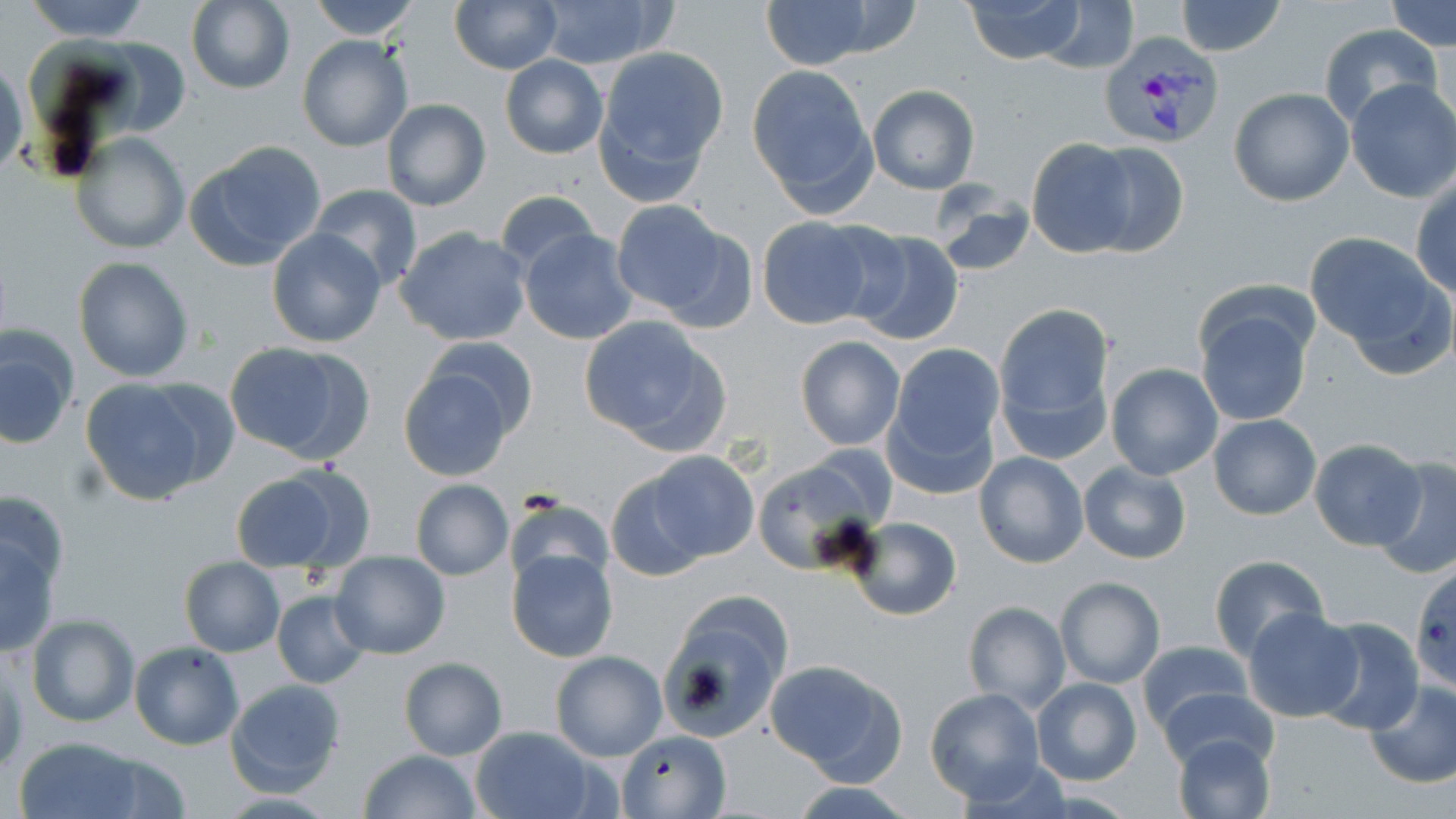

Approximate bounding boxes as named x1/y1/x2/y2 corners in pixels. Uninfected red blood cell locations: (x1=22, y1=0, x2=155, y2=41), (x1=308, y1=0, x2=422, y2=40), (x1=531, y1=0, x2=675, y2=70), (x1=964, y1=0, x2=1088, y2=64), (x1=1173, y1=0, x2=1288, y2=56), (x1=186, y1=1, x2=294, y2=93), (x1=449, y1=1, x2=560, y2=73), (x1=757, y1=1, x2=882, y2=70), (x1=1034, y1=1, x2=1141, y2=74), (x1=1386, y1=1, x2=1455, y2=50), (x1=1317, y1=23, x2=1442, y2=129), (x1=297, y1=35, x2=415, y2=153), (x1=593, y1=45, x2=729, y2=190), (x1=500, y1=55, x2=608, y2=158), (x1=1, y1=56, x2=26, y2=184), (x1=746, y1=64, x2=878, y2=213), (x1=1344, y1=80, x2=1456, y2=203), (x1=866, y1=85, x2=980, y2=194), (x1=1228, y1=89, x2=1353, y2=207), (x1=381, y1=98, x2=492, y2=211), (x1=72, y1=133, x2=189, y2=254), (x1=1027, y1=138, x2=1133, y2=255), (x1=186, y1=141, x2=328, y2=269), (x1=1083, y1=141, x2=1189, y2=258), (x1=1411, y1=177, x2=1456, y2=301), (x1=930, y1=183, x2=1034, y2=278), (x1=308, y1=185, x2=423, y2=294), (x1=495, y1=190, x2=601, y2=276), (x1=610, y1=200, x2=742, y2=323), (x1=756, y1=217, x2=884, y2=329), (x1=266, y1=227, x2=388, y2=348), (x1=395, y1=227, x2=530, y2=346), (x1=520, y1=228, x2=638, y2=344), (x1=843, y1=229, x2=965, y2=347), (x1=1304, y1=232, x2=1450, y2=365), (x1=73, y1=256, x2=196, y2=383), (x1=991, y1=300, x2=1117, y2=463), (x1=1195, y1=306, x2=1313, y2=429), (x1=578, y1=314, x2=729, y2=452), (x1=1, y1=328, x2=77, y2=449), (x1=416, y1=334, x2=542, y2=445), (x1=794, y1=337, x2=906, y2=451), (x1=224, y1=340, x2=374, y2=465), (x1=889, y1=344, x2=1005, y2=463), (x1=397, y1=361, x2=520, y2=481), (x1=1106, y1=364, x2=1223, y2=481), (x1=80, y1=377, x2=231, y2=506), (x1=1209, y1=415, x2=1322, y2=520), (x1=1308, y1=439, x2=1427, y2=552), (x1=645, y1=451, x2=759, y2=564), (x1=975, y1=451, x2=1087, y2=568), (x1=752, y1=457, x2=882, y2=574), (x1=1374, y1=457, x2=1456, y2=580), (x1=1079, y1=461, x2=1192, y2=565), (x1=228, y1=466, x2=372, y2=575), (x1=605, y1=467, x2=712, y2=582), (x1=409, y1=479, x2=513, y2=580), (x1=0, y1=487, x2=70, y2=603), (x1=508, y1=494, x2=612, y2=591), (x1=850, y1=516, x2=962, y2=622), (x1=1, y1=530, x2=61, y2=658), (x1=506, y1=549, x2=618, y2=663), (x1=331, y1=552, x2=450, y2=658), (x1=1207, y1=556, x2=1329, y2=665), (x1=180, y1=558, x2=285, y2=657), (x1=1056, y1=576, x2=1165, y2=688), (x1=271, y1=590, x2=371, y2=689), (x1=656, y1=597, x2=788, y2=744), (x1=962, y1=602, x2=1070, y2=714), (x1=1245, y1=607, x2=1363, y2=723), (x1=26, y1=613, x2=139, y2=728), (x1=1310, y1=618, x2=1423, y2=736), (x1=1136, y1=640, x2=1250, y2=733), (x1=130, y1=641, x2=244, y2=750), (x1=549, y1=650, x2=667, y2=761), (x1=0, y1=654, x2=25, y2=773), (x1=399, y1=657, x2=506, y2=760), (x1=764, y1=659, x2=908, y2=783), (x1=1031, y1=677, x2=1142, y2=787), (x1=224, y1=678, x2=346, y2=796), (x1=1363, y1=681, x2=1456, y2=789), (x1=1157, y1=687, x2=1278, y2=773), (x1=924, y1=688, x2=1044, y2=805), (x1=470, y1=727, x2=601, y2=819), (x1=618, y1=729, x2=731, y2=817), (x1=1172, y1=733, x2=1274, y2=819), (x1=12, y1=737, x2=151, y2=819), (x1=359, y1=748, x2=483, y2=819), (x1=787, y1=782, x2=923, y2=818). Plasmodium vivax-infected red blood cell locations: (x1=1095, y1=34, x2=1225, y2=151). Slide-level diagnosis: Plasmodium vivax. May-Grünwald-Giemsa stain. One field of a larger specimen. Image is 1456×819 pixels. Thin blood film. 1000x magnification. Optical microscopy.